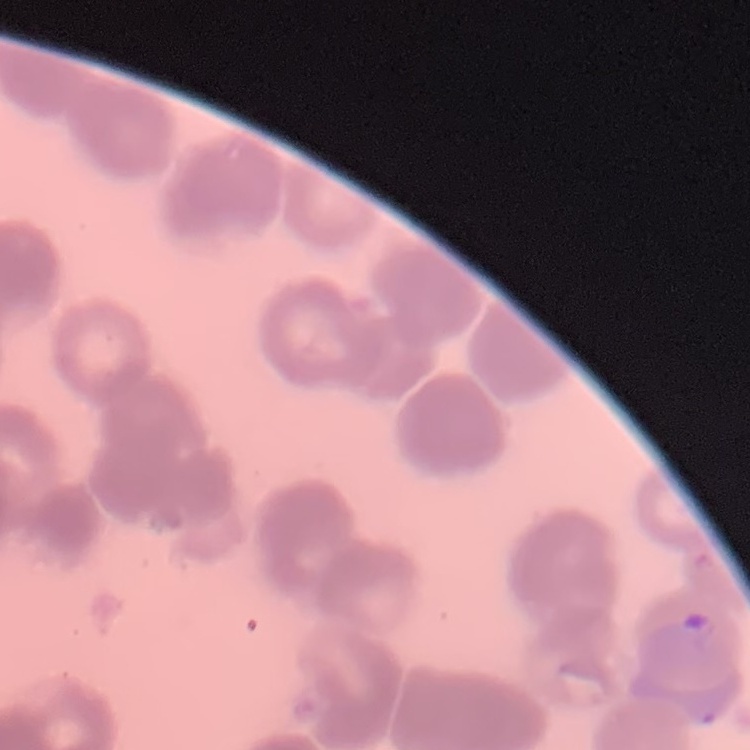

erythrocyte morphology = rouleaux formation
image type = one tile cut from a larger photomicrograph
preparation = thin blood smear
stain = Field's or Giemsa